Locate and identify every blood parasite.
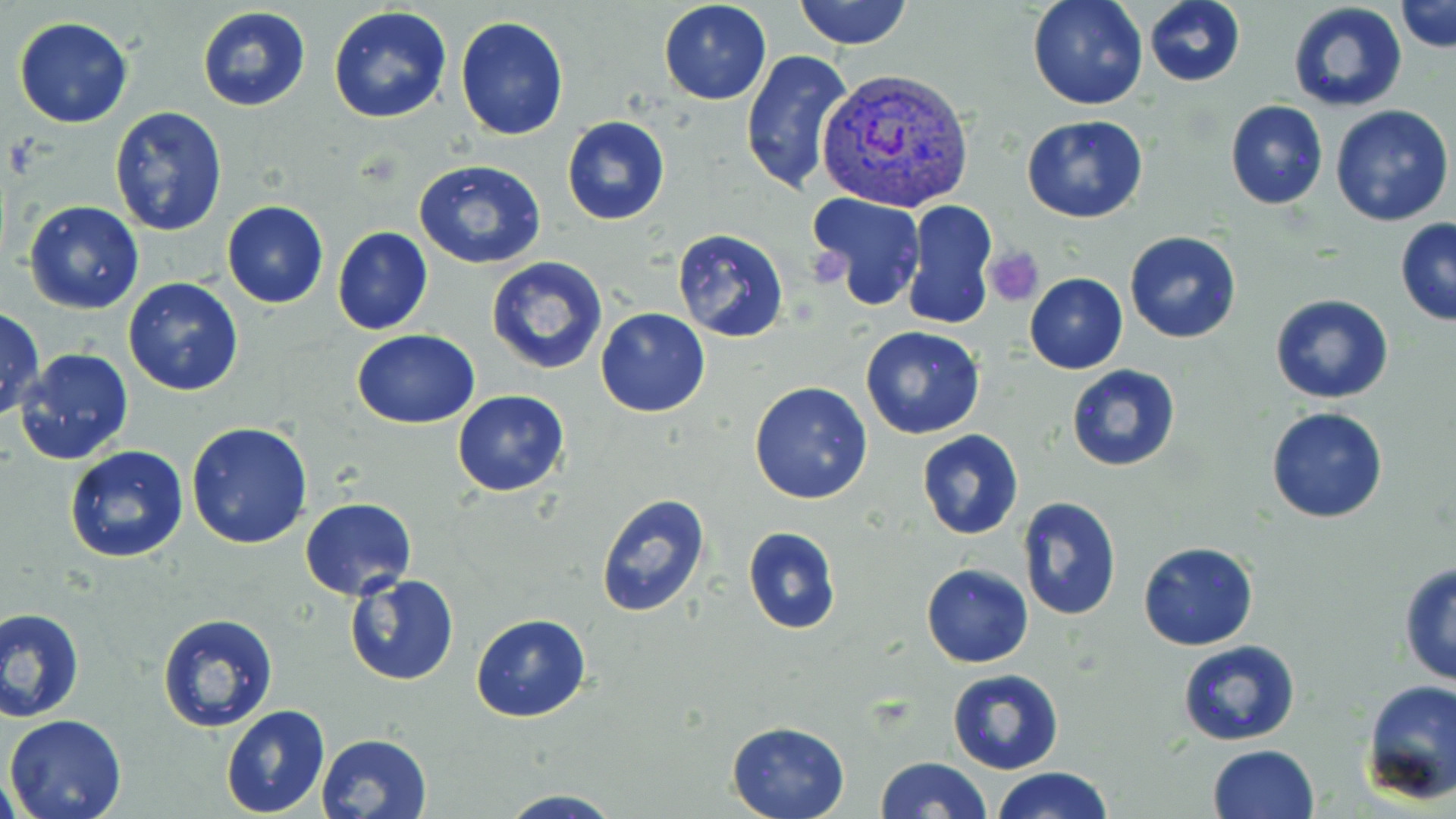
Approximate bounding boxes as (x1, y1, x2, y2) in pixels.
Plasmodium vivax-infected red blood cells: (815, 67, 977, 212).
No Plasmodium falciparum, Plasmodium ovale, Plasmodium malariae, Babesia divergens, or Trypanosoma brucei observed.

slide_level_diagnosis: Plasmodium vivax
uninfected_red_blood_cell_locations: 'approximate bounding boxes as (x1, y1, x2, y2) in pixels: (658, 0, 772, 104), (793, 0, 912, 49), (1027, 0, 1147, 110), (1144, 0, 1246, 87), (1397, 1, 1456, 53), (1285, 3, 1409, 116), (196, 7, 312, 112), (329, 7, 453, 125), (455, 15, 569, 140), (14, 18, 132, 128), (740, 47, 855, 198), (1223, 99, 1330, 210), (1330, 104, 1453, 227), (109, 106, 228, 237), (1021, 115, 1149, 222), (562, 116, 670, 224), (414, 160, 547, 270), (807, 192, 926, 311), (23, 200, 144, 314), (221, 200, 329, 308), (902, 202, 996, 330), (1394, 217, 1456, 326), (332, 227, 434, 337), (673, 228, 789, 342), (1124, 231, 1243, 344), (485, 256, 609, 375), (1023, 273, 1128, 374), (122, 276, 244, 396), (1270, 293, 1395, 404), (0, 306, 44, 419), (594, 308, 710, 417), (860, 325, 984, 439), (352, 330, 479, 428), (14, 347, 134, 465), (1066, 364, 1181, 472), (749, 381, 873, 503), (452, 390, 569, 496), (1266, 406, 1389, 525), (185, 422, 312, 549), (916, 429, 1023, 540), (64, 446, 191, 564), (593, 492, 711, 619), (1018, 496, 1122, 621), (300, 497, 416, 601), (742, 526, 841, 633), (1137, 540, 1259, 651), (1397, 561, 1456, 686), (921, 564, 1033, 668), (344, 572, 459, 687), (2, 607, 85, 721), (155, 612, 278, 735), (471, 613, 591, 722), (1177, 640, 1300, 747), (946, 669, 1064, 775), (1360, 679, 1456, 805), (220, 705, 331, 818), (4, 713, 127, 819), (725, 719, 849, 819), (316, 733, 434, 819), (1207, 744, 1320, 819), (875, 756, 991, 818), (993, 767, 1113, 819), (1, 770, 21, 819), (493, 789, 630, 819)'
magnification: 1000x
image_size: 1456×819 pixels
platelet_locations: 'approximate bounding boxes as (x1, y1, x2, y2) in pixels: (985, 246, 1044, 304)'
field_of_view: single
stain: May-Grünwald-Giemsa
modality: light microscopy
preparation: thin blood smear